Report the malaria status.
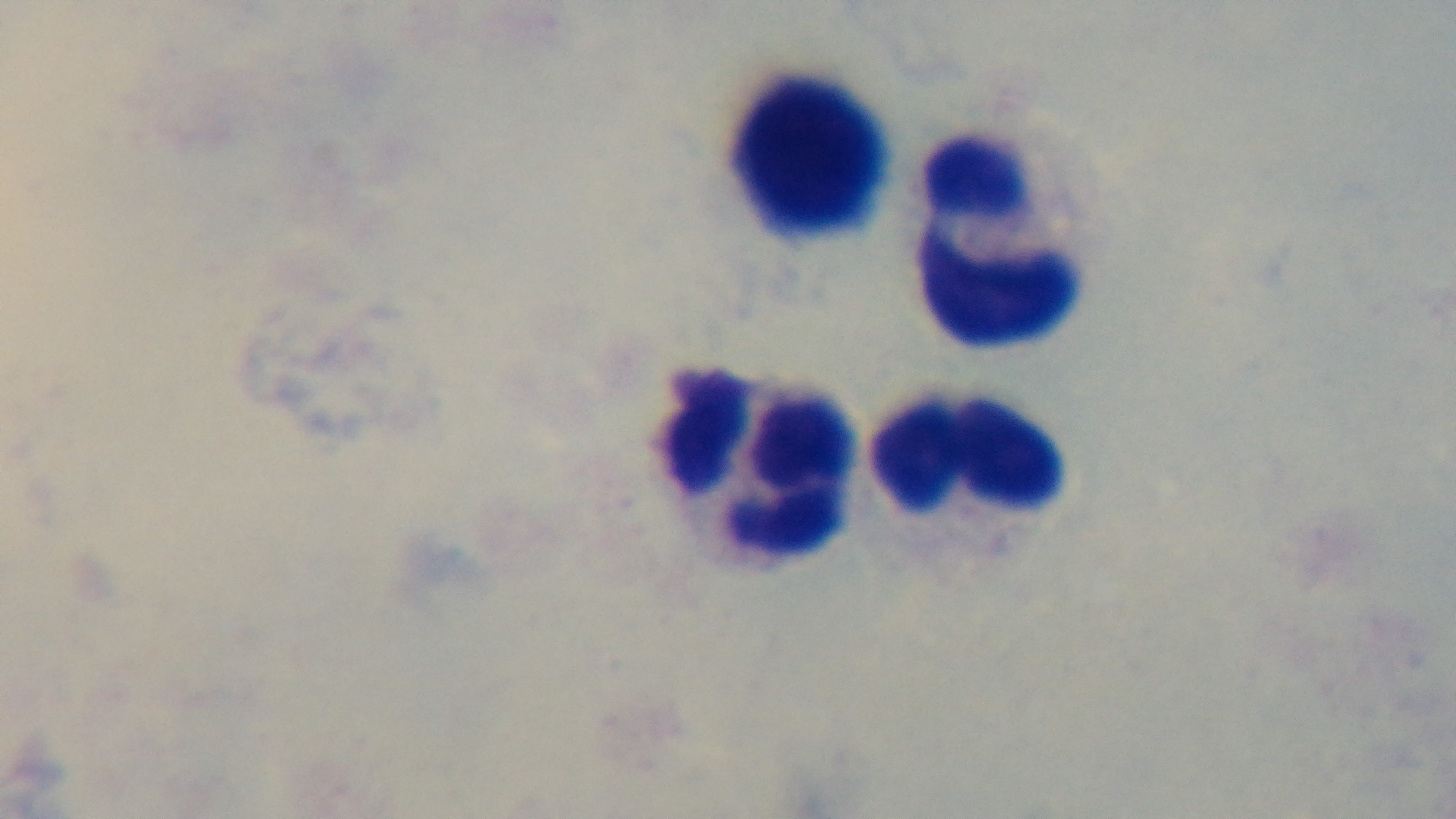
Negative.

Summary:
  - Capture: mounted 4K digital camera
  - Stain: Giemsa
  - Objective: 100x oil immersion
  - Modality: light microscopy
  - Preparation: thick
  - Field of view: single